Evaluate for Plasmodium parasites.
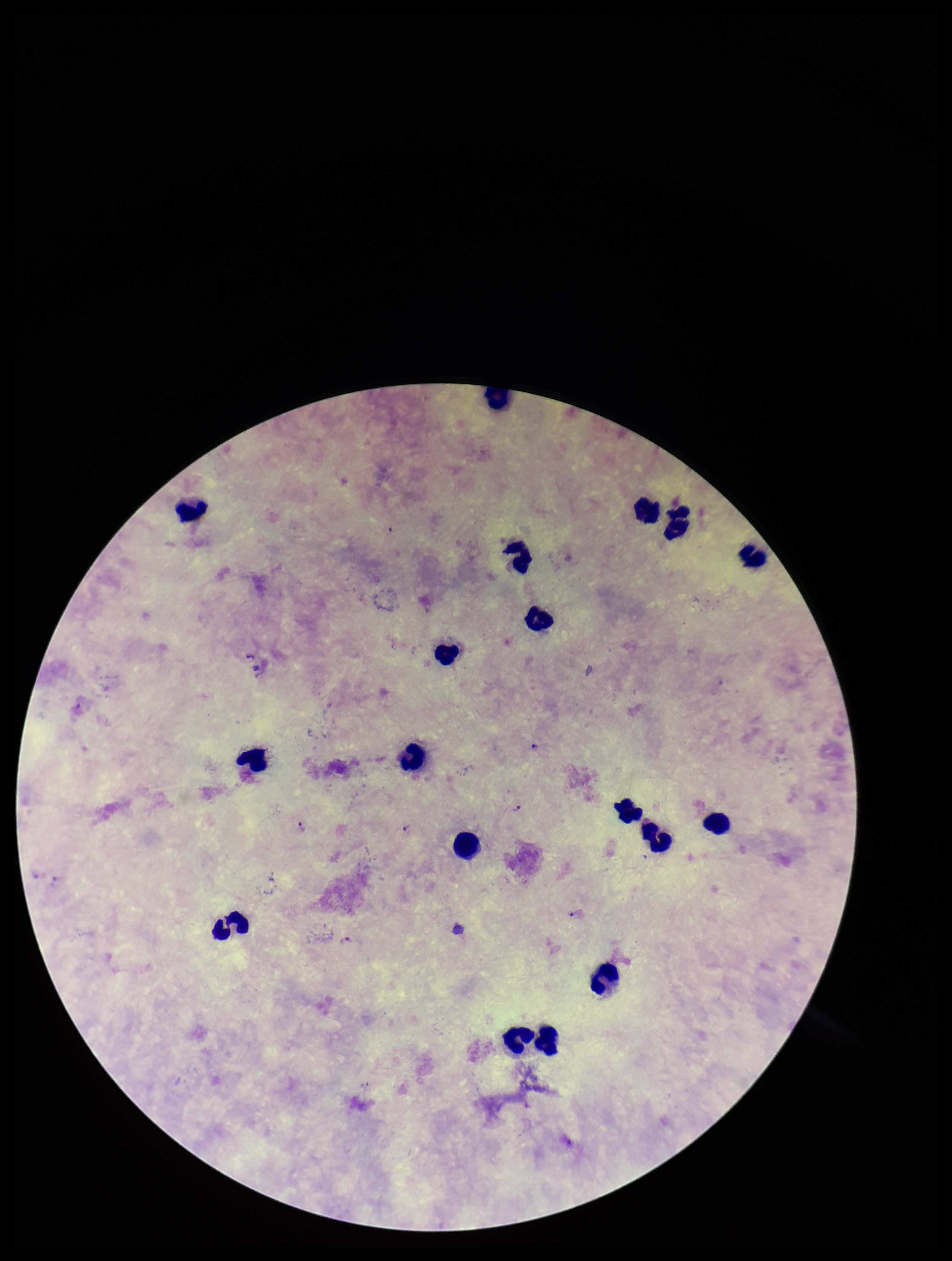

Detected.

Summary:
  - Field of view: one from this slide
  - Patient malaria status: infected
  - Capture: smartphone photograph through the microscope eyepiece
  - Preparation: thick smear
  - Leukocyte count: 18
  - Parasite count: 7
  - Species reported for this patient: Plasmodium falciparum
  - Image size: 952×1261 pixels
  - Stain: Giemsa